Name the blood parasite species.
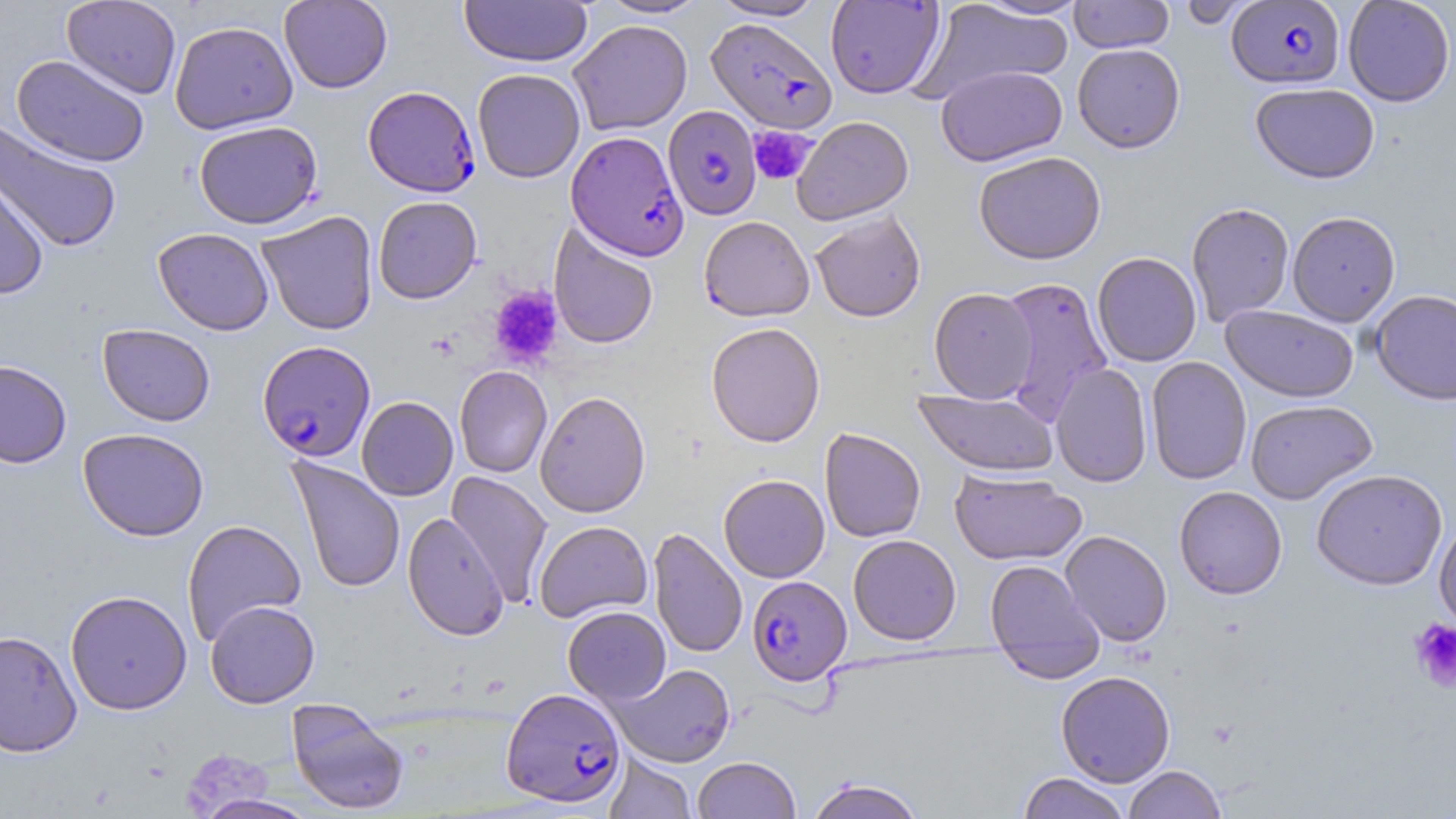

Plasmodium falciparum.

Summary:
  - Coordinate format: approximate bounding boxes as (x1,y1)-(x2,y2) corner pairs in pixels
  - Plasmodium falciparum-infected red blood cell locations: (1226,1)-(1345,88), (706,17)-(837,134), (363,86)-(480,197), (663,105)-(761,220), (566,130)-(688,261), (257,340)-(375,462), (747,576)-(851,685), (501,687)-(626,807)
  - Uninfected red blood cell locations: (62,0)-(181,99), (279,0)-(393,93), (459,0)-(592,67), (597,0)-(709,19), (710,0)-(826,21), (969,0)-(1091,19), (1069,0)-(1174,53), (1176,0)-(1258,29), (1342,0)-(1455,107), (825,1)-(945,98), (915,1)-(1073,101), (169,20)-(298,134), (568,20)-(692,135), (1072,43)-(1185,153), (12,54)-(150,167), (936,65)-(1067,166), (472,68)-(585,183), (1250,82)-(1380,183), (792,116)-(914,225), (0,120)-(122,254), (193,120)-(324,229), (973,150)-(1106,264), (0,170)-(49,300), (373,196)-(482,304), (1185,202)-(1294,326), (810,210)-(926,322), (256,211)-(379,336), (1287,211)-(1400,326), (699,216)-(814,321), (549,223)-(659,349), (153,228)-(274,335), (1092,252)-(1202,367), (996,276)-(1114,424), (929,287)-(1038,403), (1370,289)-(1456,405), (1221,305)-(1359,403), (706,322)-(825,447), (97,323)-(216,426), (1146,357)-(1252,485), (0,359)-(72,469), (1050,362)-(1153,488), (454,365)-(552,478), (913,388)-(1059,476), (535,391)-(650,518), (356,396)-(458,501), (1245,399)-(1377,504), (819,427)-(926,542), (78,428)-(210,541), (288,456)-(405,594), (948,469)-(1086,565), (1310,469)-(1448,590), (445,471)-(553,608), (718,474)-(830,582), (1174,486)-(1287,599), (402,512)-(509,641), (1434,514)-(1456,637), (181,519)-(306,647), (534,520)-(652,623), (648,527)-(747,659), (1060,530)-(1172,647), (848,534)-(961,645), (985,559)-(1104,673), (65,589)-(192,715), (205,600)-(320,708), (563,606)-(671,705), (0,629)-(82,757), (610,663)-(735,767), (1056,670)-(1175,786), (287,698)-(409,814), (605,751)-(696,819), (692,756)-(801,819), (1123,765)-(1227,818), (1018,772)-(1130,819), (805,777)-(927,819), (192,794)-(321,819)
  - Platelet locations: (747,126)-(817,186), (489,286)-(564,369), (1408,618)-(1456,693)
  - Modality: light microscopy
  - Stain: May-Grünwald-Giemsa
  - Field of view: one of a larger specimen
  - Image size: 1456×819 pixels
  - Magnification: 1000x
  - Preparation: thin blood film